Point out each Plasmodium parasite.
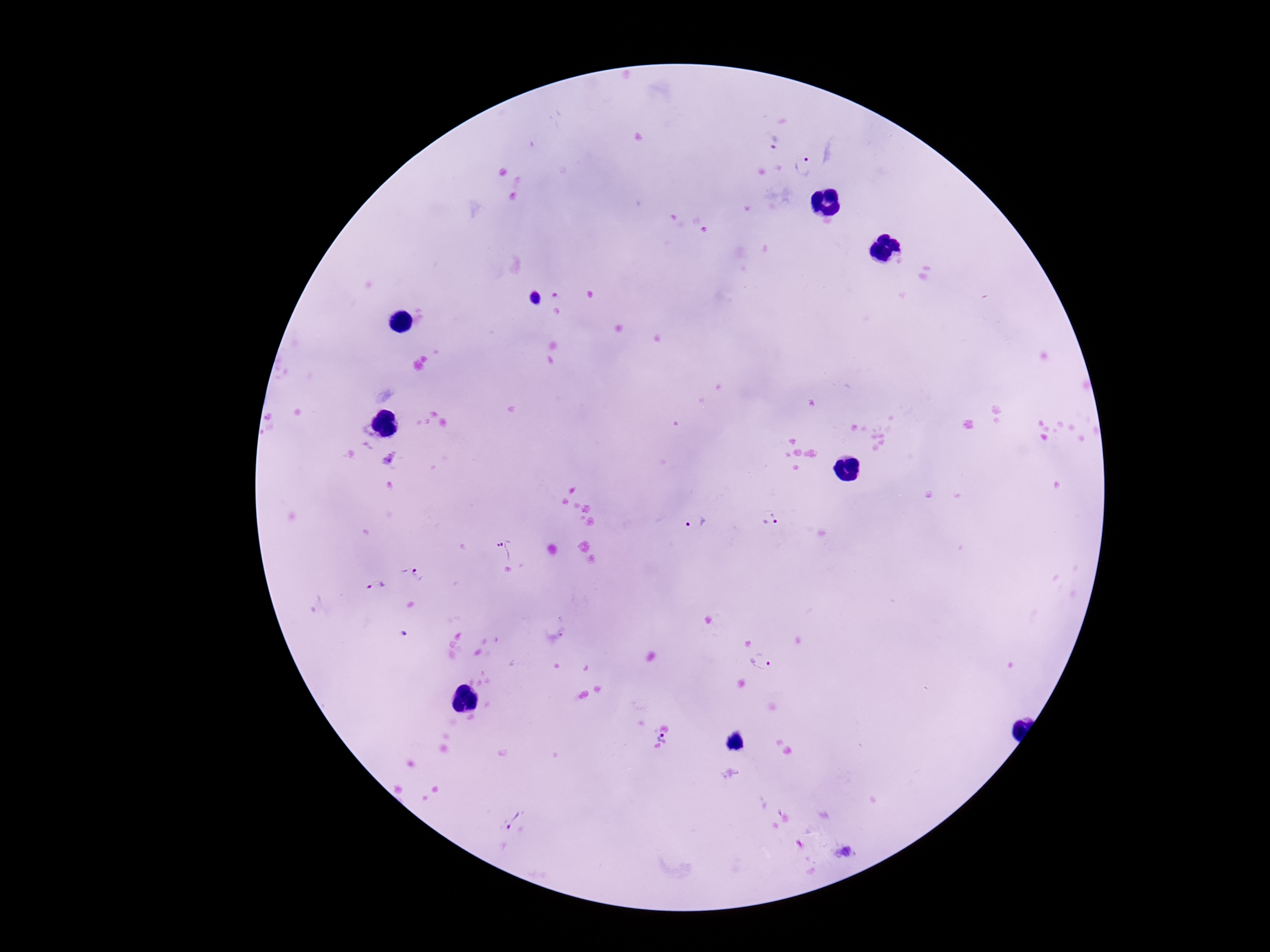

Approximate centers as [x, y] in pixels.
Plasmodium parasites: [772, 140], [805, 166], [770, 518], [696, 522], [506, 549], [416, 573], [376, 585], [397, 630], [564, 631], [763, 660], [659, 736], [512, 819], [844, 853].

Summary:
  - Stain: Giemsa
  - Patient malaria status: infected
  - Image size: 1270×952 pixels
  - Magnification: 100x
  - Field of view: one from this slide
  - Capture: smartphone camera through the microscope eyepiece
  - Preparation: thick peripheral-blood smear